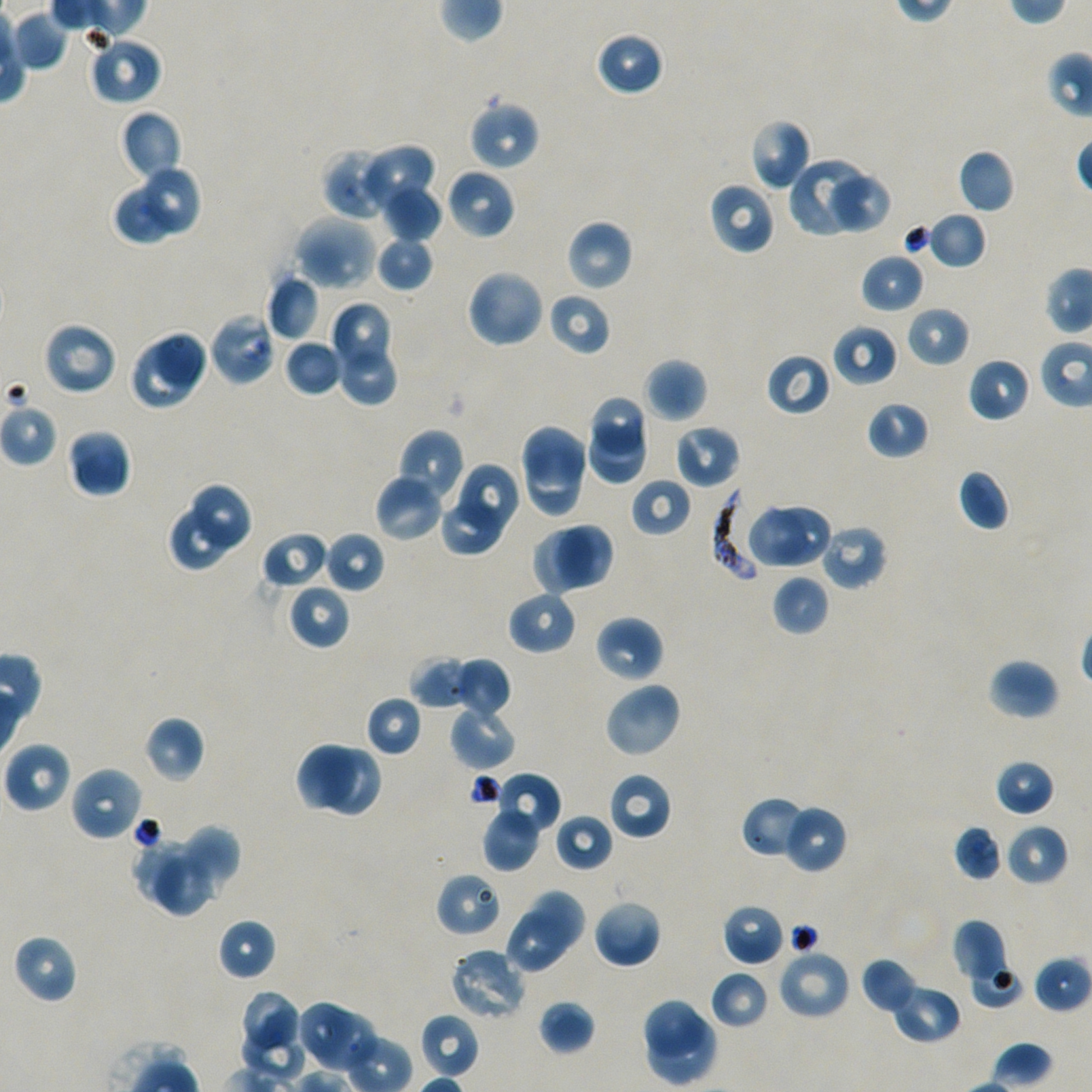
Approximate bounding boxes as [x1, y1, x2, y2] in pixels. Not every red blood cell is marked. Locations of infected red blood cells: [710, 489, 761, 583]. Locations of red blood cells of indeterminate infection status: [208, 312, 276, 386]. Locations of uninfected red blood cells: [12, 10, 69, 70], [594, 31, 663, 97], [87, 35, 162, 106], [468, 98, 540, 170], [120, 110, 182, 183], [748, 118, 812, 192], [358, 143, 436, 213], [321, 147, 393, 220], [958, 149, 1016, 214], [789, 157, 865, 236], [142, 164, 202, 235], [445, 168, 516, 240], [824, 171, 891, 234], [708, 181, 776, 255], [383, 183, 443, 244], [114, 189, 173, 244], [927, 211, 987, 269], [293, 215, 376, 292], [566, 219, 634, 292], [903, 223, 934, 259], [376, 235, 435, 291], [860, 253, 925, 312], [465, 268, 546, 349], [266, 274, 321, 341], [547, 291, 612, 356], [329, 301, 389, 371], [905, 306, 970, 367], [41, 321, 117, 396], [833, 323, 898, 387], [153, 327, 211, 389], [284, 338, 344, 397], [128, 341, 198, 412], [342, 350, 399, 407], [766, 352, 832, 416], [968, 357, 1032, 422], [643, 358, 708, 422], [592, 399, 644, 450], [866, 401, 929, 460], [0, 403, 59, 467], [519, 423, 587, 486], [589, 424, 649, 487], [675, 424, 741, 489], [67, 428, 132, 498], [395, 429, 465, 507], [524, 455, 586, 517], [456, 463, 517, 534], [957, 469, 1011, 532], [374, 473, 444, 543], [630, 477, 693, 539], [193, 482, 253, 549], [439, 499, 502, 556], [745, 505, 809, 570], [771, 505, 831, 568], [169, 507, 231, 572], [558, 522, 613, 587], [818, 524, 888, 590], [530, 528, 593, 596], [261, 530, 330, 590], [324, 531, 384, 594], [772, 574, 830, 637], [287, 583, 351, 650], [507, 589, 578, 655], [594, 615, 664, 684], [410, 654, 474, 710], [452, 657, 512, 719], [987, 658, 1059, 721], [603, 681, 682, 759], [365, 695, 422, 757], [449, 700, 517, 770], [143, 716, 204, 783], [3, 741, 72, 813], [295, 741, 354, 812], [326, 747, 380, 816], [994, 759, 1055, 817], [69, 765, 144, 842], [495, 771, 561, 833], [608, 771, 672, 841], [740, 796, 811, 859], [782, 805, 848, 874], [482, 806, 541, 872], [555, 814, 614, 871], [952, 823, 1004, 881], [1004, 823, 1069, 887], [178, 824, 242, 892], [134, 837, 206, 904], [156, 857, 213, 916], [435, 871, 503, 938], [527, 888, 587, 951], [593, 897, 662, 969], [721, 903, 786, 967], [503, 913, 568, 977], [217, 917, 276, 981], [951, 920, 1008, 985], [12, 934, 77, 1004], [448, 947, 528, 1023], [776, 948, 851, 1021], [1034, 953, 1091, 1013], [860, 956, 920, 1015], [970, 959, 1023, 1008], [709, 969, 770, 1030], [890, 983, 961, 1044], [242, 989, 303, 1049], [642, 998, 708, 1053], [296, 999, 350, 1060], [538, 1000, 596, 1055], [316, 1008, 374, 1070], [420, 1013, 480, 1078], [642, 1018, 718, 1087], [242, 1026, 307, 1078]. Single field of view. Donor blood group A+/O+. Image is 1092×1092 pixels. 100x oil-immersion objective, numerical aperture 1.45. Static in-vitro culture of P. falciparum strain NF54. Thin blood film. Giemsa-stained preparation.